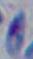

Summary:
  - Identification: Toxoplasma gondii
  - Modality: photomicrograph
  - Magnification: 1000x